Evaluate for malaria.
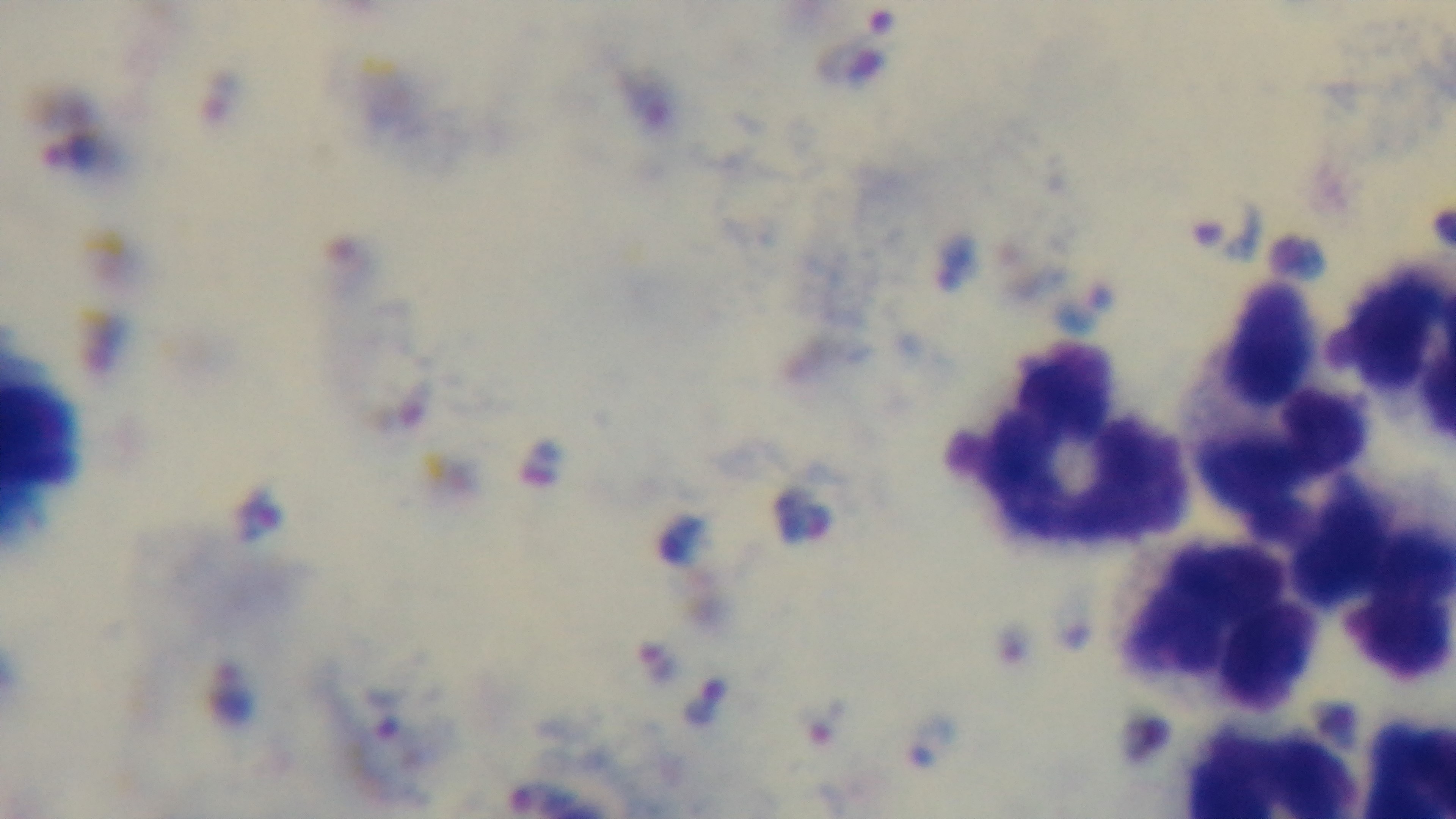
Positive.

Oil-immersion objective, 100x. Single field of view. Preparation: thick blood film. Giemsa-stained. Captured with a mounted 4K digital camera. Light microscopy.